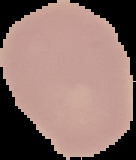
image_size: 136×160 pixels
preparation: thin blood smear
malaria_status: uninfected
image_type: segmented cell region with the area outside set to black